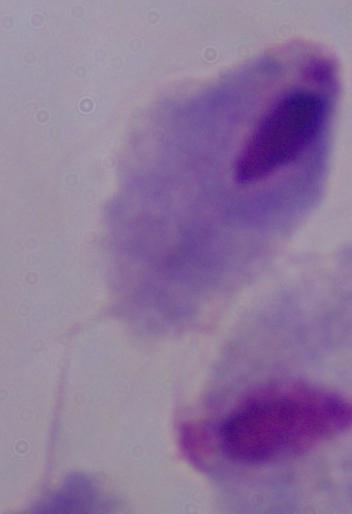

Micrograph. 1000x magnification. A trichomonad is seen.